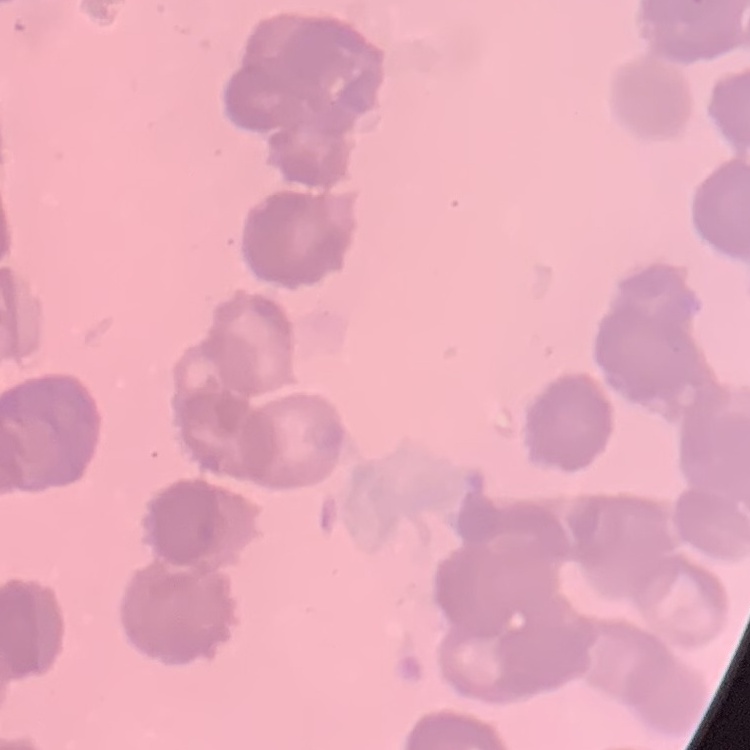 The erythrocytes show rouleaux formation. Stained with either Field's or Giemsa. Thin blood smear. Square crop of a larger photomicrograph.